Describe the morphology of the red blood cells.
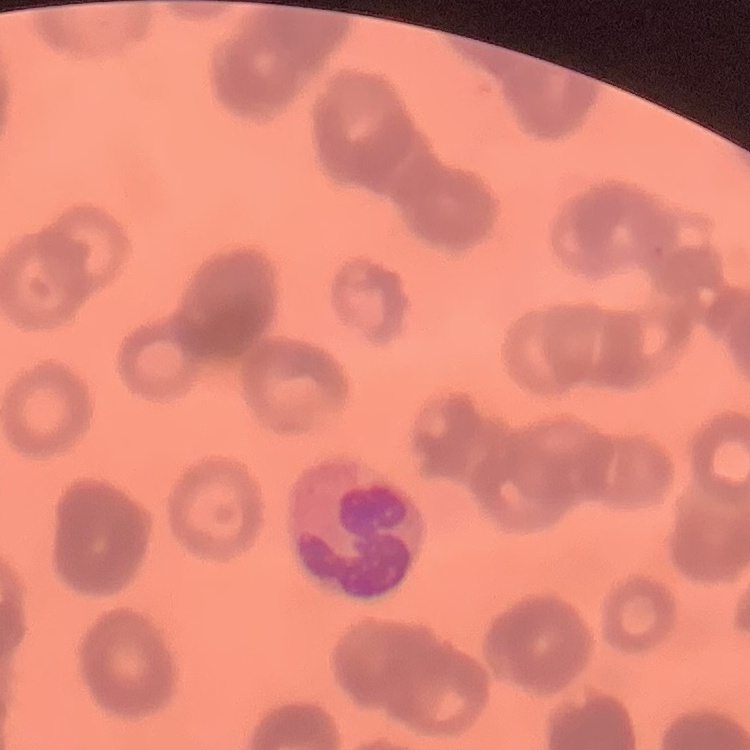
Rouleaux formation.

Thin blood smear. Square crop of a larger photomicrograph. Stained with either Field's or Giemsa.